State which cell type is depicted.
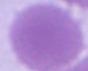
This is an erythrocyte.

Captured at 1000x magnification. Photomicrograph.